Assess this cell for malaria.
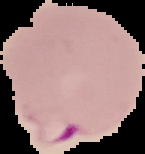
Parasitized.

Summary:
  - Image size: 145×154 pixels
  - Image type: segmented cell region with the area outside set to black
  - Preparation: thin blood smear